Assess for malaria.
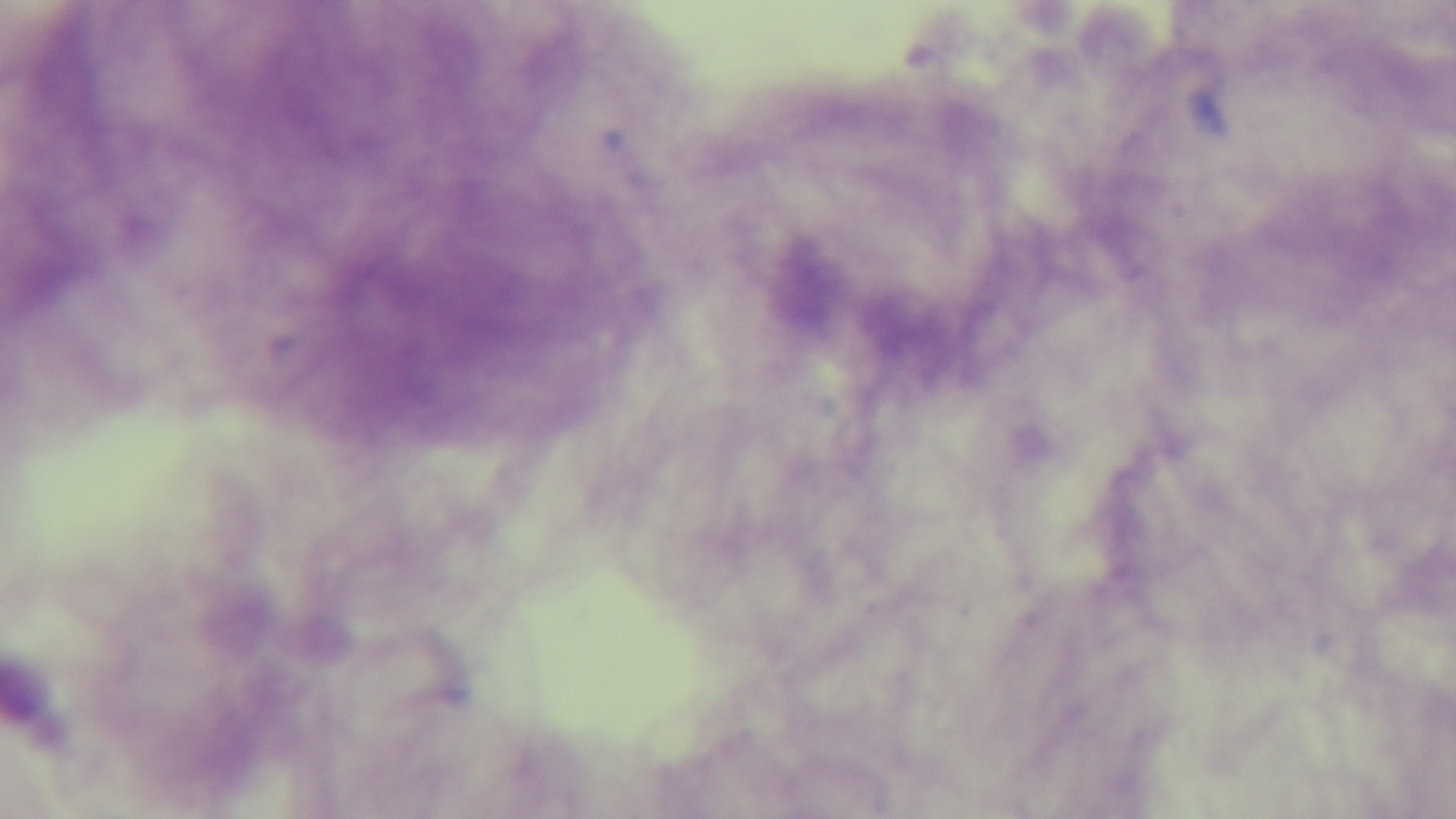

It is uninfected.

Summary:
  - Capture: mounted 4K digital camera
  - Stain: Giemsa
  - Objective: 100x oil immersion
  - Preparation: thick smear
  - Field of view: single
  - Modality: light microscopy